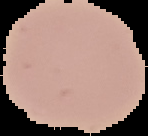

{
  "result": "no malaria parasites seen",
  "image_size": "148×136 pixels",
  "image_type": "segmented cell region with the area outside set to black",
  "preparation": "thin blood smear"
}